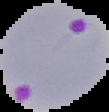

malaria status = parasitized
image type = cell region segmented out of the field of view; surrounding area masked to black
image size = 109×112 pixels
preparation = thin blood film